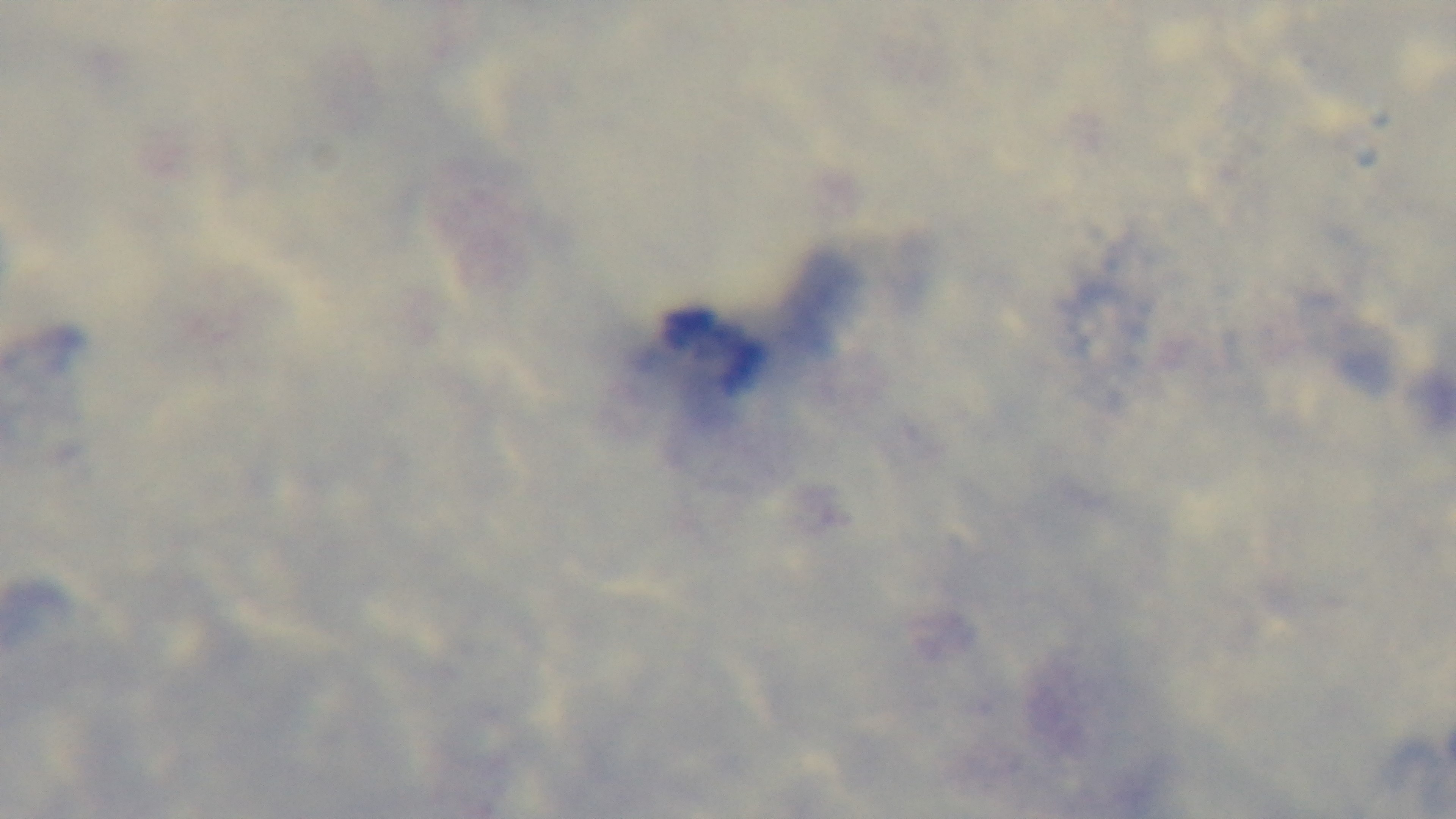
Summary:
  - Modality: light microscopy
  - Field of view: single
  - Stain: Giemsa
  - Malaria status: uninfected
  - Objective: 100x oil immersion
  - Preparation: thick smear
  - Capture: mounted 4K digital camera